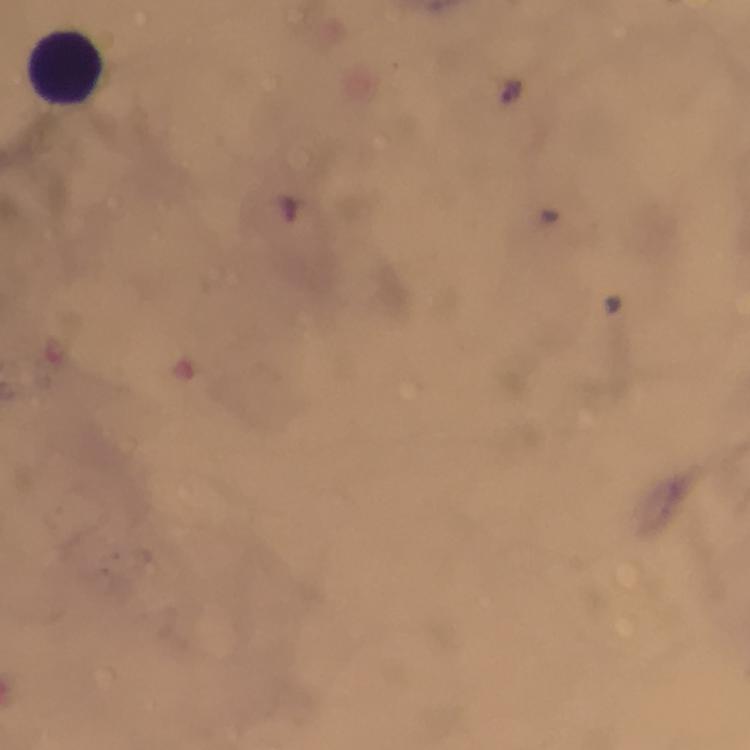
Approximate centers as (x, y) in pixels.
Summary:
  - Plasmodium parasite locations: (512, 91)
  - Leukocyte locations: (65, 69)
  - Capture: smartphone camera through the microscope
  - Magnification: 100x
  - Cropped from: one field of view
  - Context: from a diagnostic examination for malaria
  - Immersion oil: used
  - Image size: 750×750 pixels
  - Preparation: thick smear
  - Stain: Giemsa